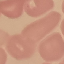

{
  "malaria_status": "uninfected",
  "stain": "Giemsa",
  "capture": "smartphone camera at the microscope eyepiece",
  "image_type": "automatically extracted cell patch, resized to 64 × 64 pixels",
  "preparation": "thin blood film"
}